Name the parasite shown.
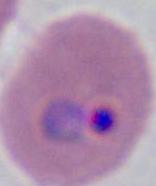
This is Plasmodium.

Summary:
  - Modality: photomicrograph
  - Magnification: 400x or 1000x